Point out each leukocyte.
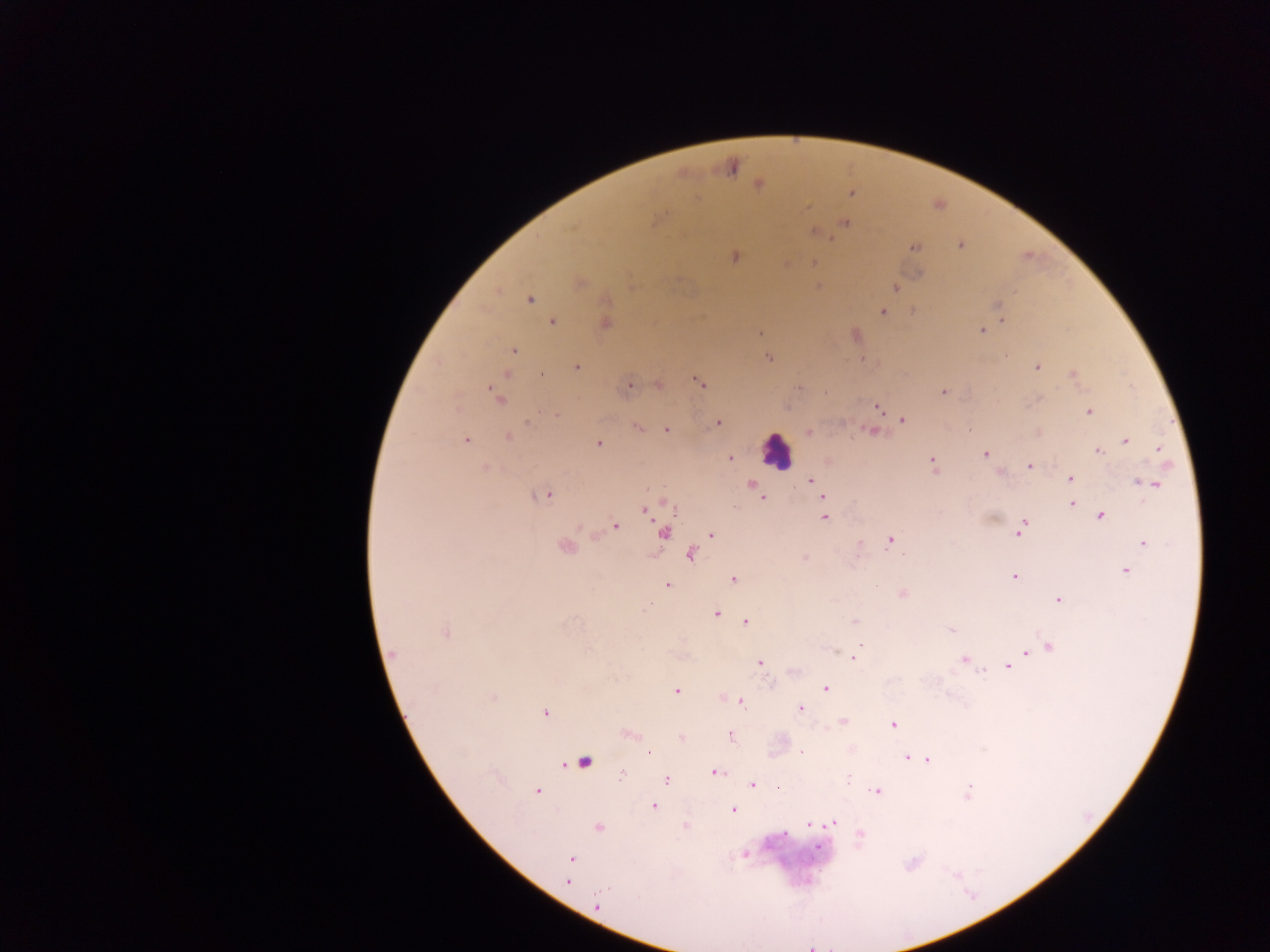
Approximate centers as x y in pixels.
Leukocytes: 776 449.

Malaria parasite locations: 758 184; 852 192; 659 219; 845 223; 816 233; 960 246; 914 247; 734 257; 814 263; 819 286; 896 287; 530 300; 606 301; 997 305; 883 312; 1003 320; 552 322; 605 324; 982 331; 760 333; 514 350; 1005 355; 769 358; 577 367; 1037 367; 1073 374; 541 375; 505 376; 699 383; 659 385; 628 386; 798 388; 943 391; 496 395; 877 406; 1089 412; 557 415; 902 420; 717 423; 638 428; 667 430; 809 432; 872 432; 509 437; 466 440; 1126 441; 598 444; 1158 450; 1098 451; 986 454; 730 459; 932 462; 1029 466; 485 467; 1070 478; 812 480; 1144 483; 751 485; 1154 485; 546 495; 823 497; 763 498; 1071 504; 645 510; 1100 516; 823 517; 615 525; 1023 526; 664 533; 712 534; 890 541; 1144 543; 564 546; 690 555; 903 555; 804 557; 1125 571; 1014 577; 733 579; 668 585; 903 594; 1058 599; 649 606; 716 613; 855 621; 746 622; 950 630; 445 634; 860 645; 1049 647; 1026 652; 394 654; 854 658; 964 659; 760 663; 1008 666; 982 672; 826 688; 677 690; 493 698; 742 703; 800 708; 545 713; 843 721; 893 724; 630 734; 681 737; 730 737; 802 752; 650 753; 907 758; 917 759; 928 760; 584 762; 716 772; 621 776; 666 780; 847 781; 752 785; 779 788; 969 789; 877 791; 537 792; 653 806; 733 810; 833 823; 809 825; 685 826; 598 827; 784 833; 860 834; 818 848; 744 855; 571 859; 568 881; 598 905. Collected in Ghana. Thick blood film. Image is 1270×952 pixels. Photographed through a microscope with a mobile-phone camera. Single field of view.